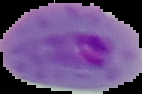 From a thin blood smear. Malaria status: parasitized. Image is 142×94 pixels. Cell region segmented out of the field of view; the surrounding area is masked to black.